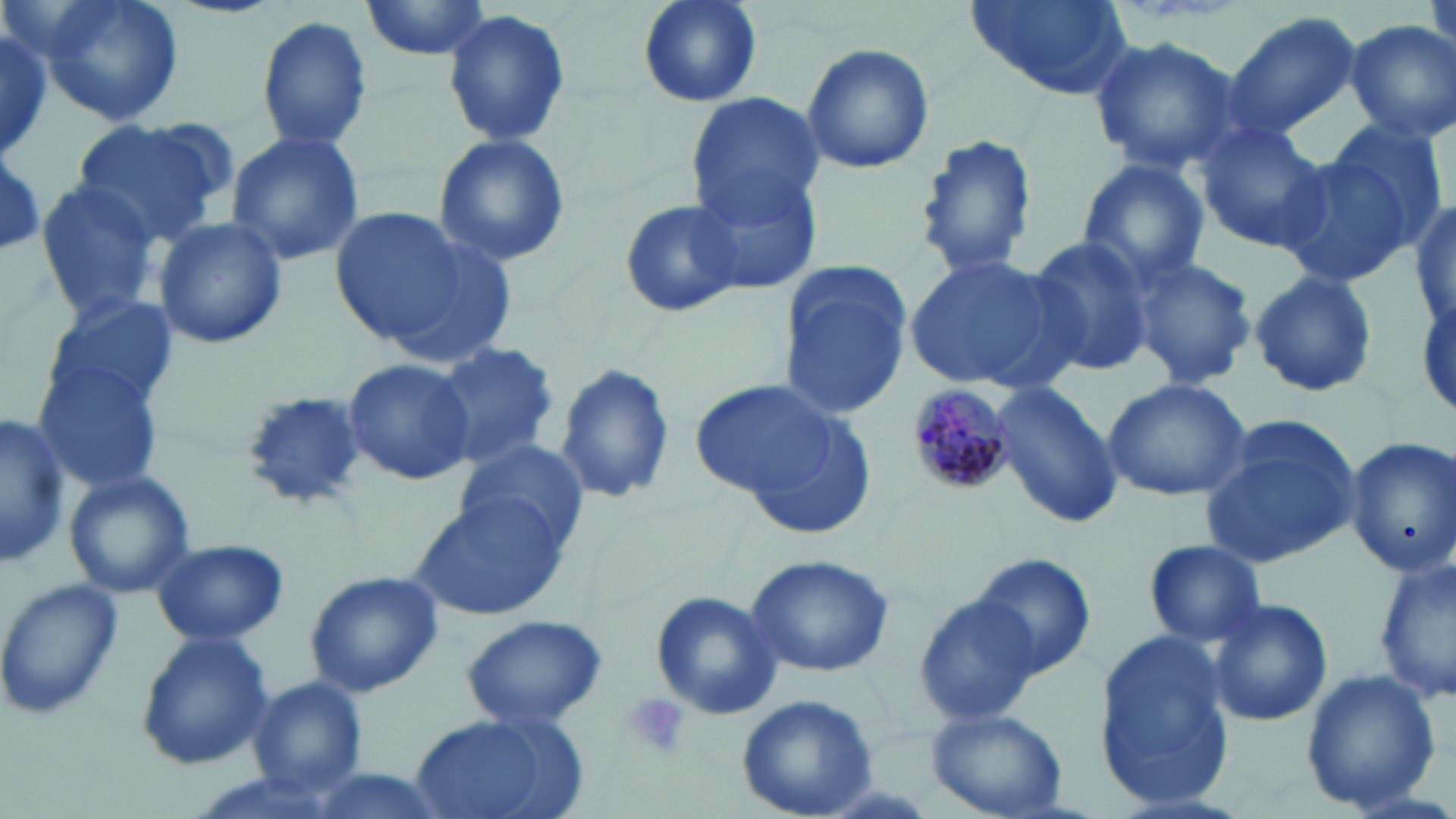
slide-level diagnosis = Plasmodium malariae
stain = May-Grünwald-Giemsa
preparation = thin blood smear
magnification = 1000x
field of view = single
Plasmodium malariae-infected red blood cell locations = approximate bounding boxes as named x1/y1/x2/y2 corners in pixels: (x1=907, y1=384, x2=1010, y2=496)
modality = light microscopy
image size = 1456×819 pixels
platelet locations = approximate bounding boxes as named x1/y1/x2/y2 corners in pixels: (x1=623, y1=693, x2=688, y2=761)
uninfected red blood cell locations = approximate bounding boxes as named x1/y1/x2/y2 corners in pixels: (x1=29, y1=0, x2=186, y2=130), (x1=360, y1=0, x2=494, y2=61), (x1=632, y1=0, x2=765, y2=109), (x1=965, y1=0, x2=1131, y2=99), (x1=1426, y1=0, x2=1456, y2=62), (x1=443, y1=8, x2=575, y2=147), (x1=1227, y1=11, x2=1362, y2=134), (x1=258, y1=15, x2=373, y2=152), (x1=0, y1=22, x2=53, y2=160), (x1=1345, y1=22, x2=1455, y2=140), (x1=1088, y1=37, x2=1247, y2=174), (x1=800, y1=42, x2=935, y2=177), (x1=686, y1=92, x2=824, y2=221), (x1=73, y1=116, x2=230, y2=244), (x1=1326, y1=116, x2=1452, y2=249), (x1=1195, y1=122, x2=1331, y2=254), (x1=225, y1=128, x2=366, y2=266), (x1=912, y1=131, x2=1037, y2=280), (x1=432, y1=133, x2=571, y2=266), (x1=1271, y1=150, x2=1413, y2=288), (x1=1, y1=157, x2=47, y2=254), (x1=1075, y1=158, x2=1211, y2=287), (x1=691, y1=166, x2=821, y2=295), (x1=34, y1=179, x2=163, y2=318), (x1=620, y1=197, x2=744, y2=318), (x1=1410, y1=202, x2=1456, y2=333), (x1=328, y1=205, x2=500, y2=355), (x1=151, y1=215, x2=290, y2=351), (x1=1024, y1=235, x2=1156, y2=379), (x1=1124, y1=253, x2=1259, y2=390), (x1=904, y1=254, x2=1078, y2=393), (x1=776, y1=260, x2=912, y2=420), (x1=1246, y1=270, x2=1381, y2=399), (x1=42, y1=294, x2=181, y2=414), (x1=433, y1=343, x2=559, y2=471), (x1=343, y1=357, x2=476, y2=487), (x1=35, y1=360, x2=167, y2=493), (x1=554, y1=361, x2=676, y2=506), (x1=687, y1=377, x2=851, y2=513), (x1=1101, y1=378, x2=1251, y2=501), (x1=990, y1=380, x2=1123, y2=529), (x1=238, y1=392, x2=372, y2=511), (x1=1198, y1=414, x2=1362, y2=569), (x1=0, y1=415, x2=70, y2=569), (x1=1344, y1=436, x2=1454, y2=577), (x1=454, y1=442, x2=588, y2=552), (x1=64, y1=469, x2=196, y2=600), (x1=411, y1=495, x2=573, y2=623), (x1=148, y1=538, x2=292, y2=648), (x1=1141, y1=539, x2=1269, y2=649), (x1=969, y1=552, x2=1095, y2=681), (x1=746, y1=554, x2=892, y2=679), (x1=1376, y1=554, x2=1456, y2=704), (x1=303, y1=569, x2=444, y2=699), (x1=0, y1=576, x2=125, y2=723), (x1=650, y1=591, x2=782, y2=721), (x1=914, y1=593, x2=1046, y2=727), (x1=1205, y1=597, x2=1332, y2=726), (x1=461, y1=614, x2=609, y2=732), (x1=136, y1=630, x2=274, y2=769), (x1=1094, y1=630, x2=1237, y2=809), (x1=1300, y1=669, x2=1440, y2=813), (x1=249, y1=677, x2=368, y2=798), (x1=734, y1=693, x2=880, y2=819), (x1=927, y1=707, x2=1069, y2=818), (x1=407, y1=711, x2=586, y2=819), (x1=299, y1=767, x2=450, y2=819)